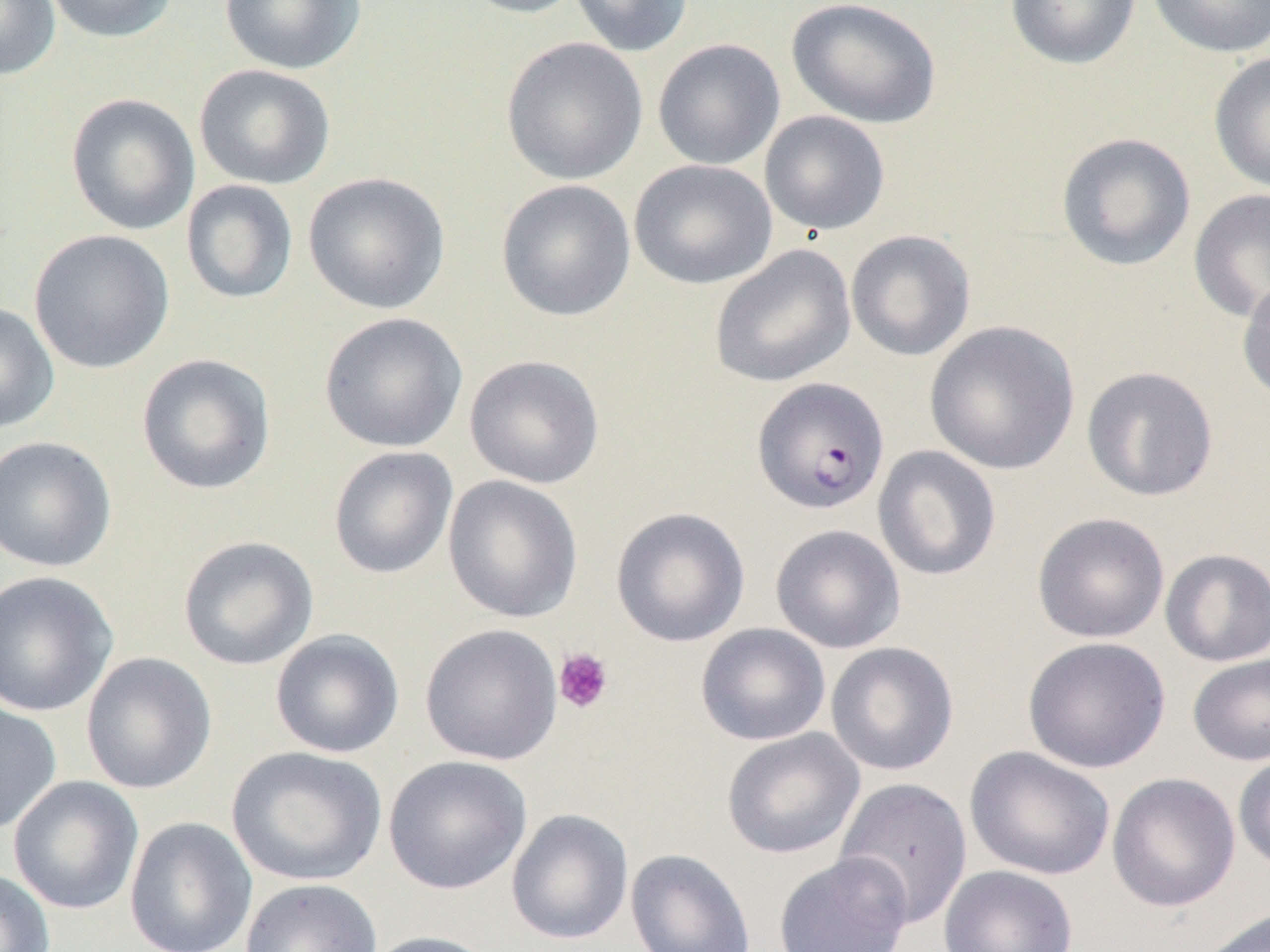
slide-level diagnosis = Plasmodium falciparum
magnification = 1000x
preparation = thin blood smear
platelet locations = approximate bounding boxes as named x1/y1/x2/y2 corners in pixels: (x1=553, y1=647, x2=614, y2=714)
modality = optical microscopy
field of view = one of a larger specimen
Plasmodium falciparum-infected red blood cell locations = approximate bounding boxes as named x1/y1/x2/y2 corners in pixels: (x1=751, y1=377, x2=890, y2=515)
image size = 1270×952 pixels
uninfected red blood cell locations = approximate bounding boxes as named x1/y1/x2/y2 corners in pixels: (x1=0, y1=0, x2=61, y2=81), (x1=43, y1=0, x2=179, y2=44), (x1=218, y1=0, x2=366, y2=75), (x1=457, y1=0, x2=588, y2=19), (x1=569, y1=0, x2=693, y2=57), (x1=786, y1=0, x2=942, y2=129), (x1=1004, y1=0, x2=1142, y2=70), (x1=1146, y1=0, x2=1270, y2=59), (x1=501, y1=36, x2=648, y2=185), (x1=652, y1=38, x2=785, y2=170), (x1=1209, y1=50, x2=1270, y2=194), (x1=193, y1=64, x2=336, y2=190), (x1=66, y1=93, x2=200, y2=235), (x1=759, y1=110, x2=890, y2=236), (x1=1055, y1=132, x2=1197, y2=272), (x1=629, y1=159, x2=777, y2=290), (x1=302, y1=171, x2=451, y2=314), (x1=181, y1=179, x2=299, y2=304), (x1=496, y1=179, x2=636, y2=322), (x1=1189, y1=188, x2=1270, y2=322), (x1=28, y1=229, x2=175, y2=375), (x1=845, y1=230, x2=976, y2=361), (x1=709, y1=244, x2=857, y2=389), (x1=1237, y1=275, x2=1270, y2=404), (x1=0, y1=301, x2=60, y2=434), (x1=319, y1=312, x2=468, y2=454), (x1=924, y1=320, x2=1081, y2=475), (x1=136, y1=353, x2=277, y2=495), (x1=464, y1=355, x2=605, y2=489), (x1=1081, y1=366, x2=1219, y2=502), (x1=0, y1=435, x2=117, y2=573), (x1=872, y1=445, x2=1001, y2=581), (x1=328, y1=446, x2=458, y2=579), (x1=443, y1=475, x2=583, y2=623), (x1=610, y1=506, x2=750, y2=647), (x1=1031, y1=512, x2=1170, y2=643), (x1=770, y1=524, x2=906, y2=654), (x1=177, y1=535, x2=319, y2=671), (x1=1160, y1=548, x2=1270, y2=667), (x1=0, y1=570, x2=119, y2=718), (x1=420, y1=623, x2=563, y2=766), (x1=695, y1=623, x2=831, y2=746), (x1=270, y1=628, x2=404, y2=758), (x1=1022, y1=636, x2=1171, y2=774), (x1=825, y1=641, x2=959, y2=776), (x1=81, y1=652, x2=217, y2=794), (x1=1187, y1=652, x2=1270, y2=766), (x1=0, y1=702, x2=62, y2=833), (x1=721, y1=728, x2=865, y2=859), (x1=226, y1=746, x2=387, y2=886), (x1=964, y1=746, x2=1115, y2=880), (x1=1232, y1=751, x2=1270, y2=874), (x1=383, y1=755, x2=532, y2=894), (x1=1107, y1=772, x2=1240, y2=913), (x1=8, y1=775, x2=144, y2=915), (x1=834, y1=777, x2=973, y2=928), (x1=506, y1=808, x2=634, y2=945), (x1=124, y1=816, x2=258, y2=952), (x1=625, y1=848, x2=756, y2=952), (x1=773, y1=852, x2=913, y2=952), (x1=938, y1=865, x2=1078, y2=952), (x1=0, y1=868, x2=55, y2=952), (x1=239, y1=878, x2=383, y2=952), (x1=1196, y1=906, x2=1270, y2=952), (x1=362, y1=930, x2=503, y2=952)